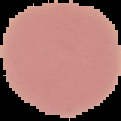 The area outside the segmented cell region is set to black. Result: negative for malaria parasites. From a thin blood smear. Image is 121×121 pixels.